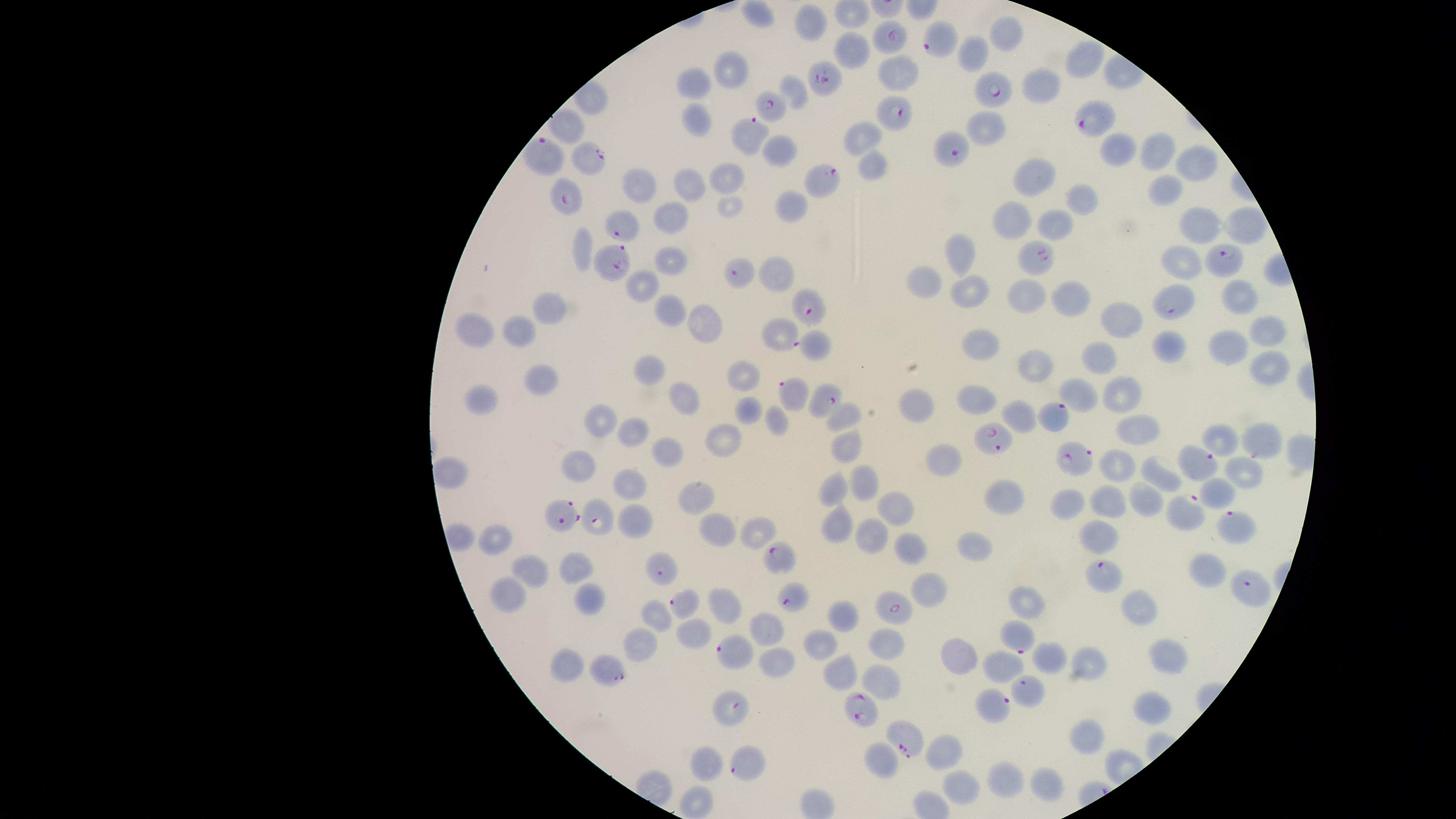

Approximate marker points as {x, y} in pixels.
Summary:
  - Uninfected red blood cells: {757, 10}, {811, 23}, {1007, 36}, {852, 51}, {977, 54}, {1087, 55}, {731, 67}, {897, 75}, {692, 81}, {1041, 86}, {694, 123}, {985, 123}, {571, 124}, {864, 137}, {782, 147}, {1117, 149}, {1160, 154}, {1195, 166}, {871, 168}, {1040, 174}, {727, 181}, {637, 184}, {685, 185}, {1170, 193}, {1081, 198}, {795, 203}, {727, 208}, {677, 216}, {1012, 220}, {1195, 223}, {1241, 223}, {1055, 227}, {584, 245}, {963, 254}, {671, 258}, {1183, 262}, {782, 269}, {645, 284}, {928, 284}, {969, 290}, {1237, 295}, {1028, 296}, {1070, 297}, {547, 307}, {665, 310}, {1120, 318}, {702, 323}, {473, 328}, {1264, 328}, {521, 332}, {816, 343}, {1165, 345}, {977, 346}, {1226, 346}, {1103, 357}, {1267, 365}, {644, 366}, {1040, 368}, {745, 375}, {540, 377}, {684, 395}, {1122, 395}, {1082, 396}, {479, 399}, {975, 403}, {749, 406}, {916, 406}, {849, 413}, {1020, 417}, {600, 419}, {775, 422}, {1135, 429}, {633, 430}, {1221, 435}, {725, 436}, {844, 440}, {667, 450}, {943, 459}, {1116, 464}, {579, 465}, {454, 472}, {1248, 475}, {1159, 476}, {629, 480}, {869, 484}, {833, 491}, {1219, 491}, {691, 493}, {1105, 498}, {1006, 499}, {1140, 499}, {1071, 504}, {893, 508}, {638, 520}, {714, 524}, {749, 528}, {837, 528}, {873, 534}, {1095, 536}, {496, 543}, {910, 547}, {975, 547}, {528, 566}, {576, 567}, {1207, 568}, {927, 590}, {508, 593}, {591, 599}, {726, 599}, {1025, 603}, {1142, 610}, {653, 613}, {846, 614}, {690, 628}, {770, 628}, {823, 637}, {884, 642}, {641, 645}, {953, 657}, {1173, 657}, {1053, 660}, {563, 664}, {778, 664}, {1003, 667}, {1094, 668}, {846, 671}, {882, 681}, {1153, 708}, {1089, 736}, {945, 754}, {709, 760}, {884, 760}, {1007, 781}, {1042, 784}, {963, 788}, {693, 801}
  - Parasitized red blood cells: {936, 37}, {893, 38}, {825, 79}, {999, 86}, {771, 111}, {892, 114}, {1092, 122}, {754, 134}, {947, 148}, {547, 156}, {591, 159}, {824, 177}, {567, 198}, {627, 229}, {1222, 261}, {1039, 262}, {615, 263}, {740, 273}, {1171, 303}, {805, 311}, {781, 330}, {797, 396}, {830, 403}, {1054, 419}, {999, 441}, {1263, 443}, {1075, 461}, {1199, 467}, {565, 514}, {1180, 514}, {594, 515}, {1229, 524}, {780, 556}, {663, 570}, {1106, 574}, {1246, 586}, {790, 600}, {685, 604}, {892, 611}, {1019, 640}, {734, 655}, {610, 671}, {1023, 689}, {992, 706}, {735, 710}, {863, 714}, {910, 738}, {744, 765}
  - Species: Plasmodium falciparum
  - Image size: 1456×819 pixels
  - Preparation: thin blood film
  - Visible region: circular
  - Presence: malaria parasites seen
  - Stain: Giemsa
  - Capture: smartphone photograph through the microscope eyepiece
  - Field of view: single